Name the parasite shown.
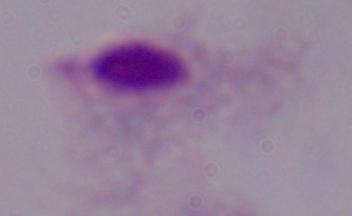
This is a trichomonad.

Summary:
  - Modality: photomicrograph
  - Magnification: 1000x